Identify the preparation type.
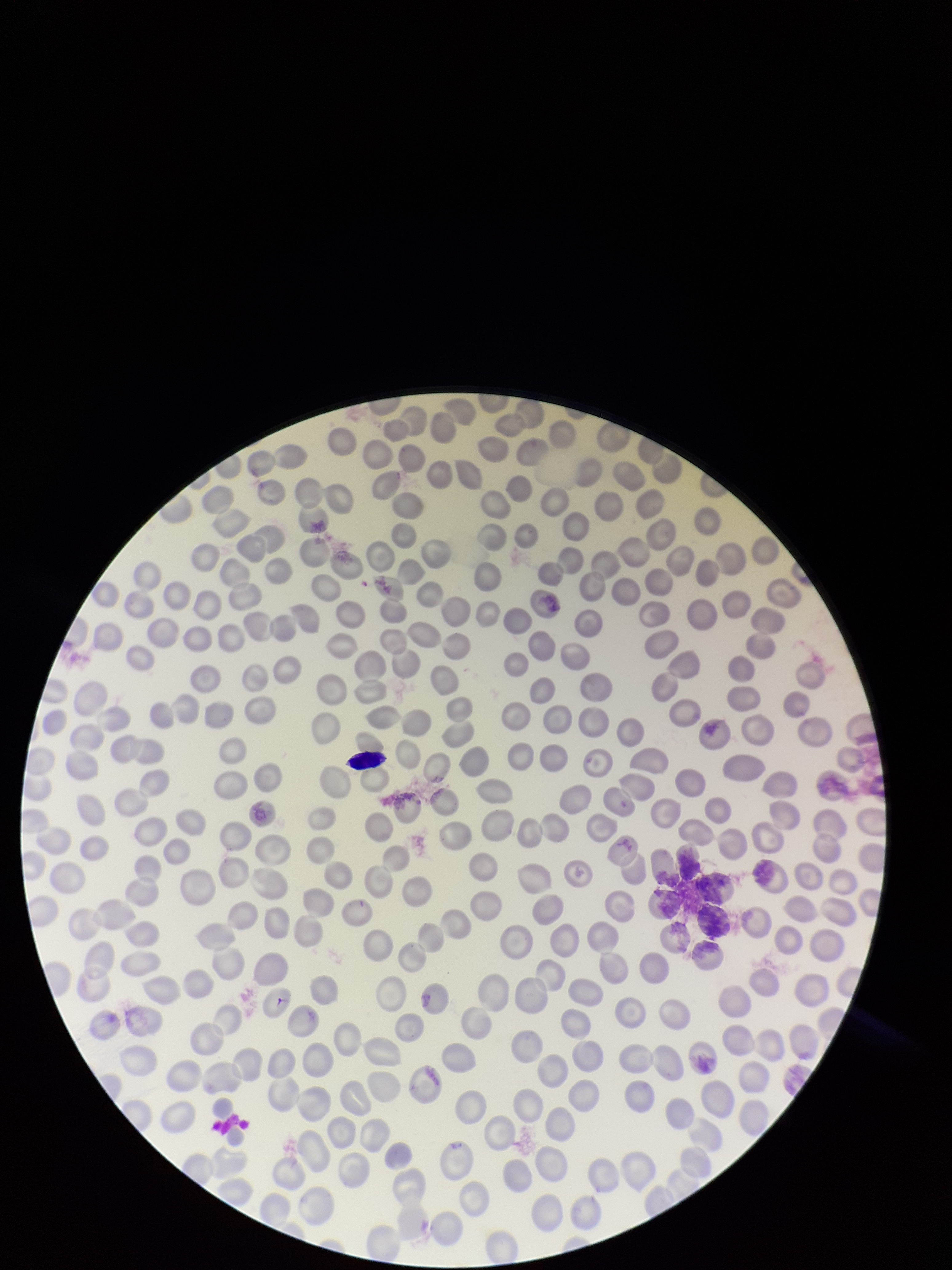

It is a thin blood smear.

field of view = single
stain = Giemsa
red blood cell count = 232
image size = 952×1270 pixels
patient malaria status = negative
parasitized red blood cell count = 0
parasitized red blood cells = none seen
capture = smartphone photograph through the microscope eyepiece